State the blood parasite species.
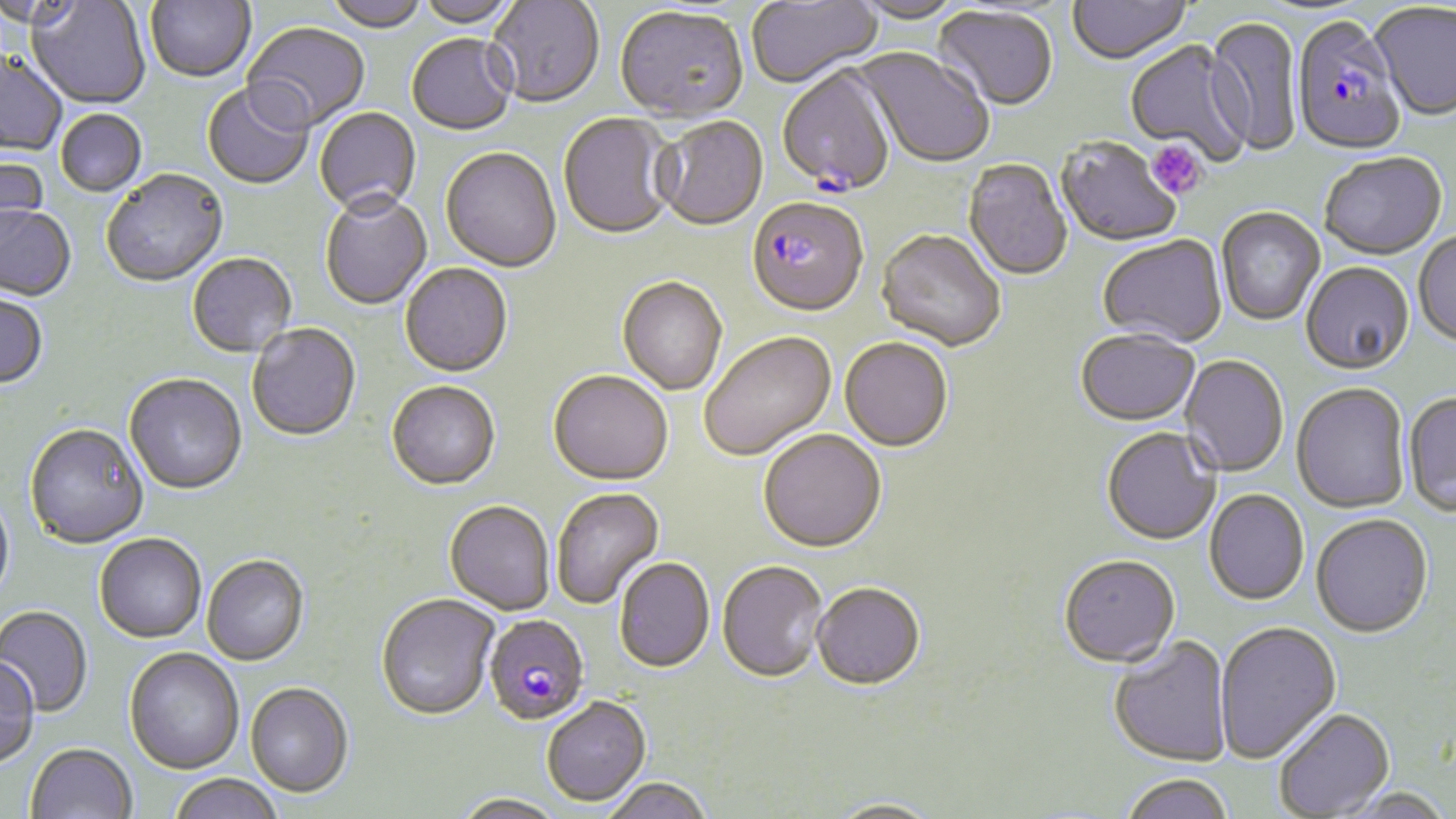
Plasmodium falciparum.

magnification = 1000x
preparation = thin blood smear
image size = 1456×819 pixels
Plasmodium falciparum-infected red blood cell locations = approximate bounding boxes as (x1,y1)-(x2,y2) corner pairs in pixels: (1292,20)-(1405,158), (777,67)-(897,197), (747,199)-(868,319), (484,615)-(589,726)
field of view = one of a larger specimen
uninfected red blood cell locations = approximate bounding boxes as (x1,y1)-(x2,y2) corner pairs in pixels: (0,0)-(85,31), (146,0)-(255,83), (324,0)-(430,34), (415,0)-(525,31), (486,0)-(605,110), (747,0)-(883,89), (27,1)-(150,109), (850,1)-(968,26), (1068,1)-(1192,68), (1371,4)-(1456,123), (615,8)-(748,125), (933,8)-(1057,113), (1205,17)-(1303,158), (242,23)-(370,134), (406,36)-(517,137), (1125,41)-(1252,164), (856,48)-(995,170), (0,53)-(68,155), (202,83)-(315,191), (314,108)-(422,218), (55,110)-(147,197), (558,114)-(676,241), (653,118)-(768,232), (1056,138)-(1182,248), (440,149)-(561,274), (0,154)-(50,251), (1319,155)-(1447,261), (963,160)-(1073,283), (101,170)-(229,289), (319,194)-(432,311), (0,207)-(76,302), (1216,208)-(1325,327), (876,231)-(1006,353), (1413,232)-(1456,350), (1097,238)-(1227,349), (188,254)-(297,359), (400,264)-(513,378), (1301,264)-(1415,377), (618,278)-(727,395), (0,293)-(48,390), (247,324)-(361,442), (1075,331)-(1200,429), (699,332)-(836,462), (840,338)-(954,453), (1180,356)-(1289,478), (548,372)-(673,487), (124,375)-(247,496), (386,382)-(500,491), (1292,384)-(1410,515), (1403,392)-(1456,518), (24,424)-(149,550), (1101,429)-(1221,547), (758,431)-(887,554), (551,487)-(664,610), (0,488)-(15,609), (1205,490)-(1309,606), (444,502)-(554,616), (1311,515)-(1434,640), (95,535)-(207,644), (202,555)-(309,666), (1058,555)-(1181,670), (614,558)-(715,674), (717,561)-(828,683), (812,583)-(925,692), (375,594)-(500,721), (0,606)-(92,717), (1214,622)-(1341,763), (1109,635)-(1233,767), (124,648)-(244,774), (0,657)-(39,769), (245,682)-(353,798), (541,697)-(650,806), (1273,708)-(1395,817), (25,743)-(137,819), (1119,773)-(1236,819), (168,774)-(283,819), (598,779)-(713,819), (1333,789)-(1456,818), (450,793)-(567,819), (825,798)-(945,818)
stain = May-Grünwald-Giemsa
platelet locations = approximate bounding boxes as (x1,y1)-(x2,y2) corner pairs in pixels: (1147,140)-(1207,200)
modality = optical microscopy